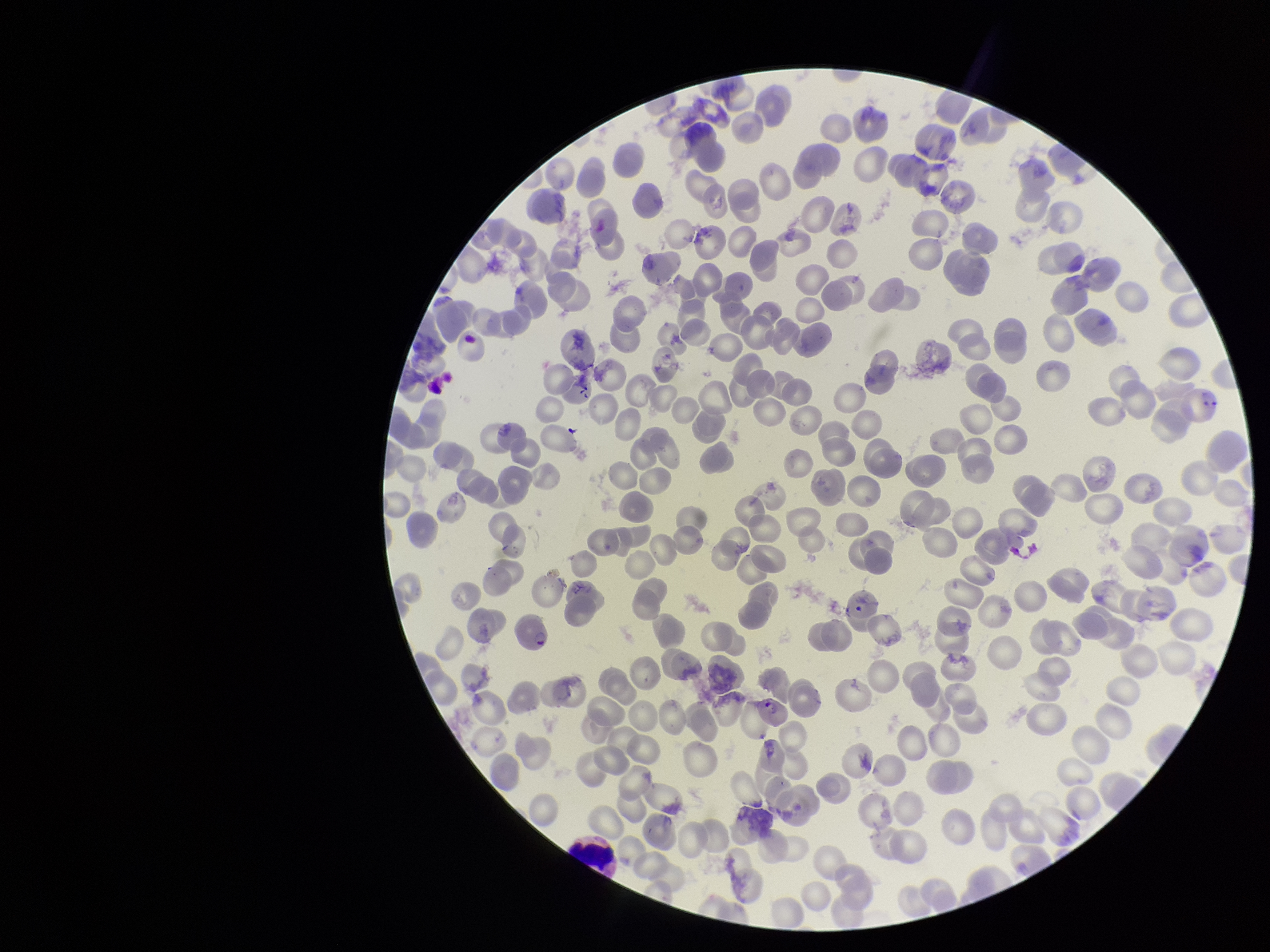

Summary:
  - Preparation: thin blood smear
  - Patient malaria status: infected
  - Stain: Giemsa
  - Field of view: one from this slide
  - Parasitized red blood cell count: 3
  - Image size: 1270×952 pixels
  - Red blood cell count: 214
  - Capture: smartphone photograph through the microscope eyepiece
  - Parasitized red blood cells: identified
  - Species reported for this patient: Plasmodium falciparum